Report the malaria status of this cell.
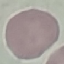

It is uninfected.

Summary:
  - Image type: cell patch, automatically extracted from a larger field of view and resized to 64 × 64 pixels
  - Stain: Giemsa
  - Capture: smartphone camera at the microscope eyepiece
  - Preparation: thin blood smear